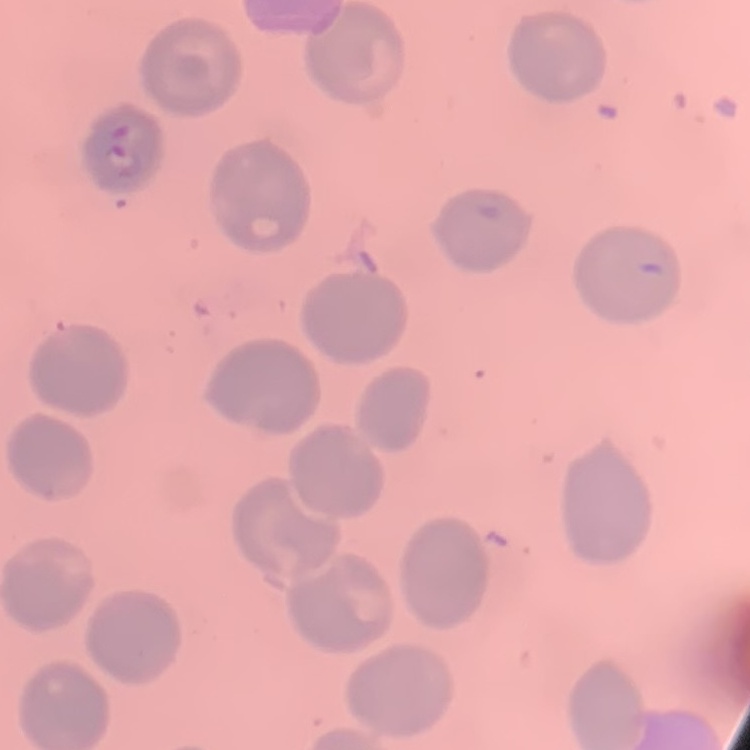

Summary:
  - Red blood cell morphology: no rouleaux formation
  - Image type: square crop of a larger photomicrograph
  - Stain: Field's or Giemsa
  - Preparation: thin peripheral smear